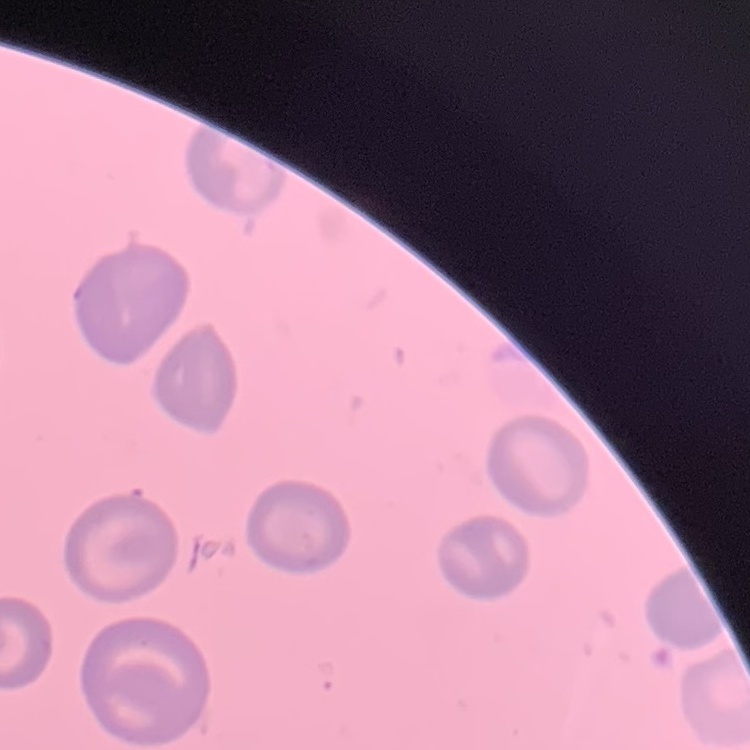
The red blood cells exhibit no rouleaux formation. Stained with either Field's or Giemsa. Thin blood smear. One tile cut from a larger photomicrograph.